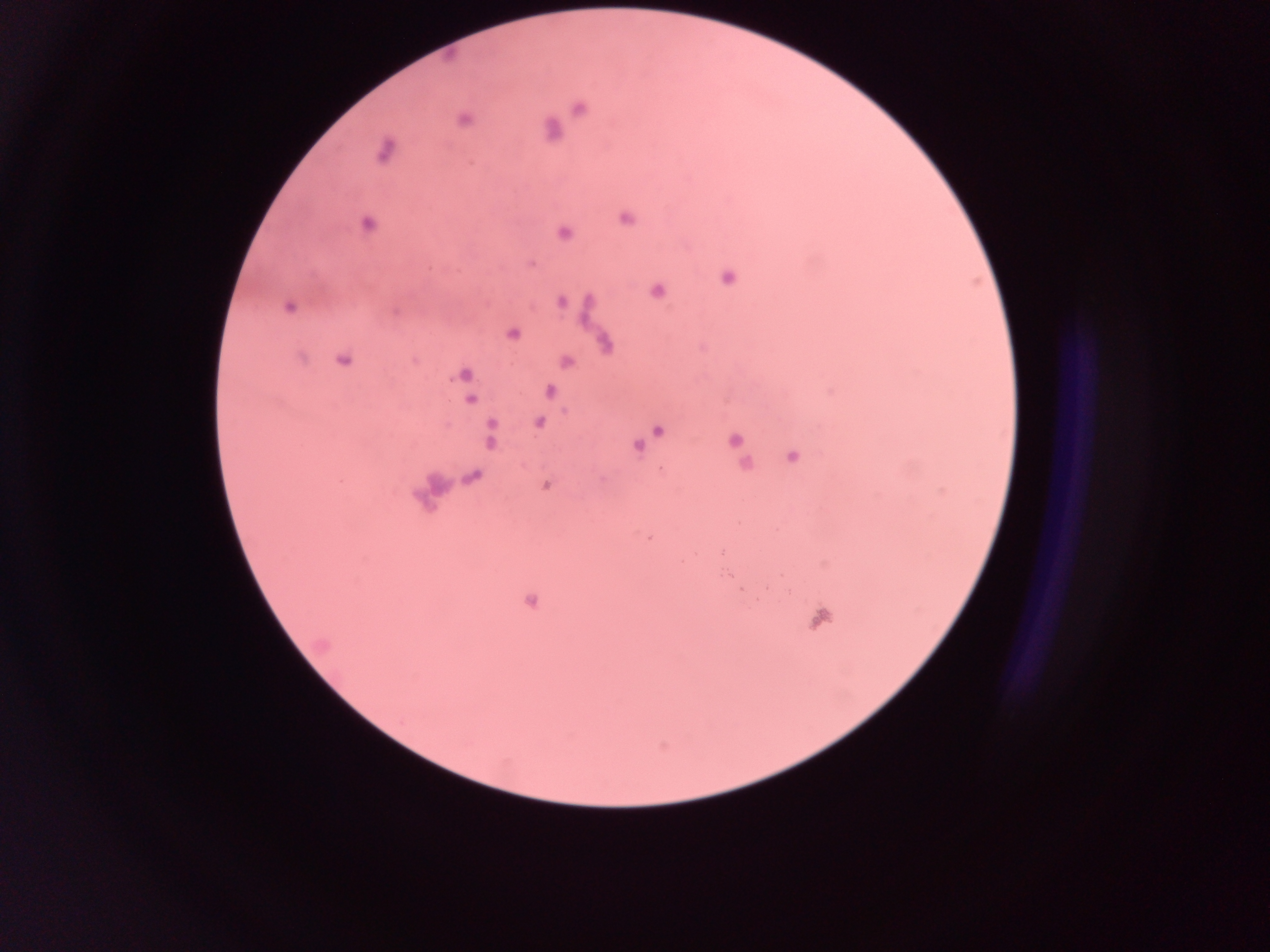 Approximate centers as {x, y} in pixels. Malaria parasite locations: {578, 108}, {463, 119}, {551, 130}, {385, 149}, {625, 217}, {367, 224}, {563, 233}, {530, 264}, {727, 277}, {656, 290}, {560, 301}, {288, 306}, {511, 334}, {604, 342}, {343, 359}, {565, 361}, {463, 374}, {466, 389}, {548, 391}, {470, 399}, {538, 422}, {657, 430}, {490, 434}, {735, 439}, {641, 442}, {637, 445}, {791, 456}, {744, 464}, {472, 477}, {545, 485}, {742, 590}, {531, 600}, {820, 618}. Sample from Ghana. Thick blood smear. Image is 1270×952 pixels. One field of view. Mobile-phone photograph taken through the microscope.